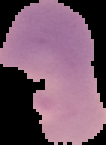
From a thin blood smear. Image is 106×145 pixels. Result: no Plasmodium parasites detected. Segmented cell region on a black background.